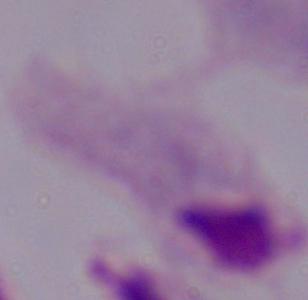
modality = photomicrograph
magnification = 1000x
identification = trichomonad